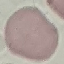

{
  "malaria_status": "uninfected",
  "preparation": "thin smear",
  "stain": "Giemsa",
  "image_type": "automatically extracted cell patch, resized to 64 × 64 pixels",
  "capture": "smartphone through the microscope eyepiece"
}